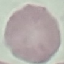

Malaria status: uninfected. Thin blood smear. Photographed with a smartphone camera at the microscope eyepiece. Automatically extracted cell patch, resized to 64 × 64 pixels. Giemsa stain.